Comment on the morphology of the red blood cells.
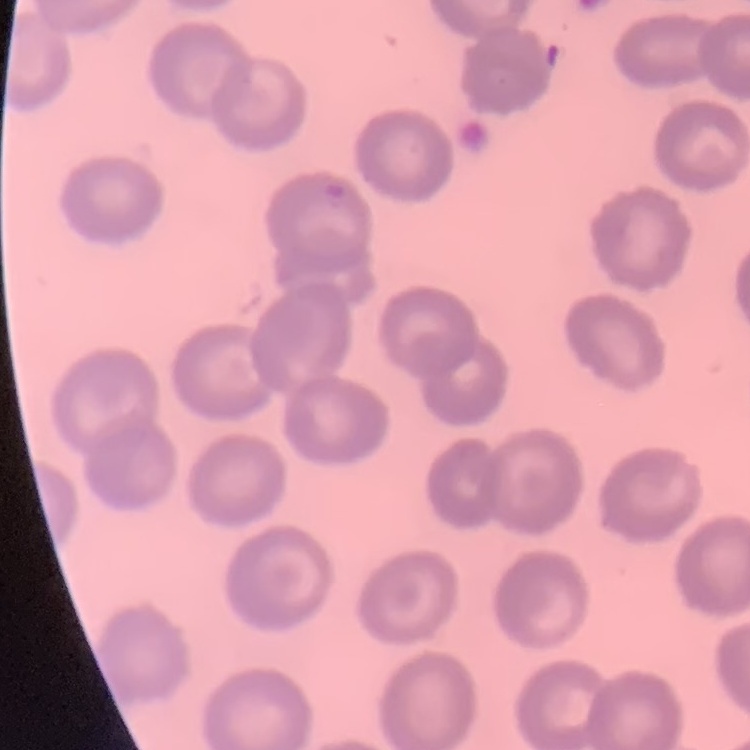

No rouleaux formation.

preparation = thin blood film
image type = one tile cut from a larger photomicrograph
stain = Field's or Giemsa